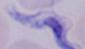
Captured at 1000x magnification. A trypanosome is shown. Micrograph.